Locate and identify every blood parasite.
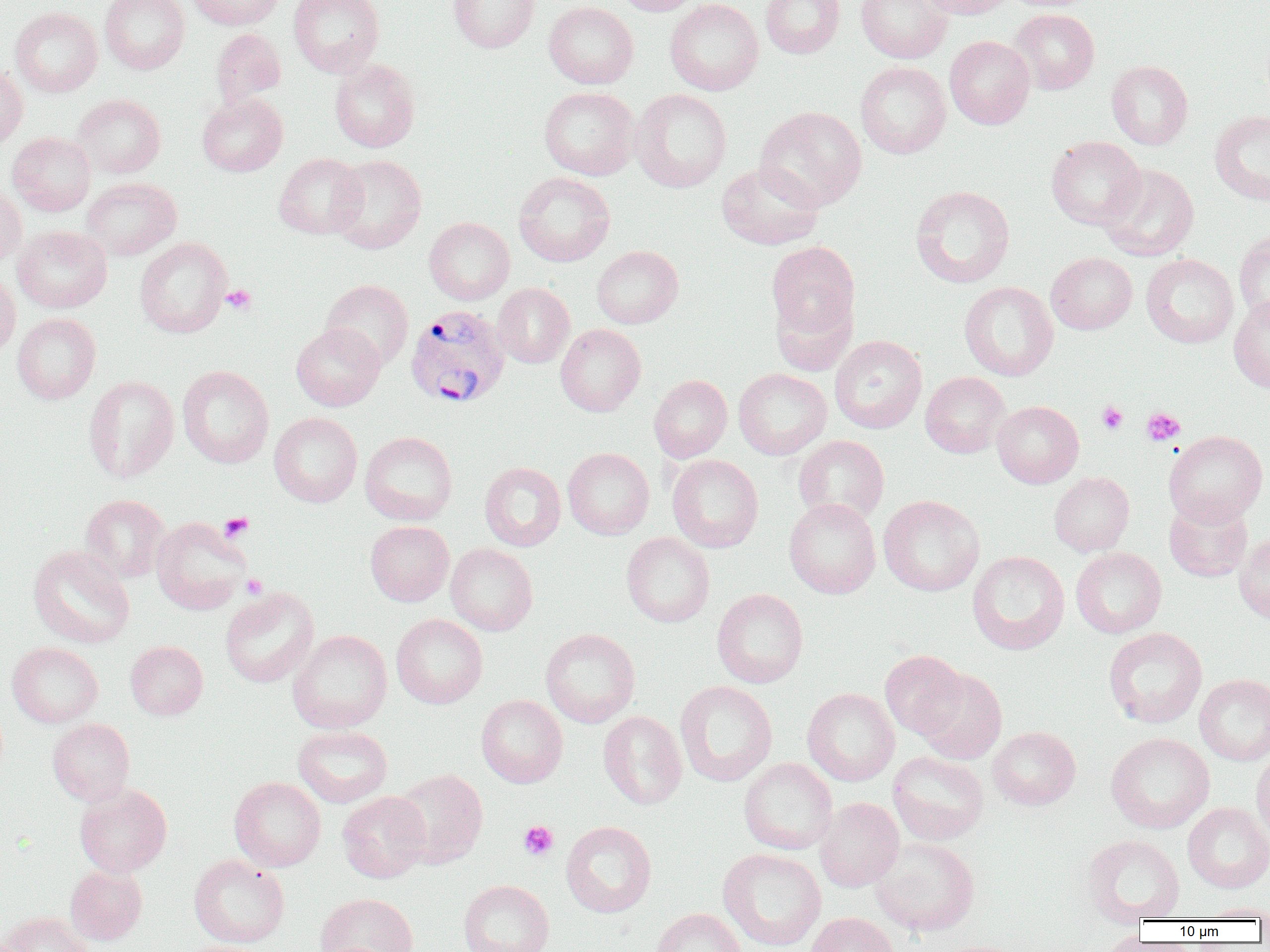
Approximate bounding boxes as (x1, y1, x2, y2) in pixels.
Plasmodium vivax-infected red blood cells: (405, 304, 511, 409).
No Plasmodium falciparum, Plasmodium ovale, Plasmodium malariae, Babesia divergens, or Trypanosoma brucei observed.

Uninfected red blood cell locations: (100, 0, 189, 74), (187, 0, 283, 29), (289, 0, 384, 77), (448, 0, 539, 53), (612, 0, 703, 16), (665, 0, 763, 95), (760, 0, 845, 58), (855, 0, 953, 63), (916, 0, 1015, 19), (543, 1, 639, 89), (10, 7, 103, 97), (1010, 9, 1100, 94), (211, 28, 286, 108), (944, 35, 1035, 129), (329, 59, 420, 152), (1106, 60, 1193, 150), (855, 61, 951, 159), (0, 65, 28, 153), (539, 87, 640, 180), (631, 89, 731, 193), (197, 93, 288, 177), (72, 94, 166, 178), (755, 106, 867, 211), (1210, 110, 1270, 205), (7, 132, 95, 216), (1046, 136, 1145, 230), (273, 153, 367, 239), (330, 154, 427, 254), (716, 163, 823, 250), (1098, 164, 1199, 261), (513, 172, 615, 267), (81, 177, 182, 260), (0, 184, 26, 269), (910, 186, 1014, 288), (424, 217, 515, 305), (13, 226, 112, 313), (1234, 230, 1270, 325), (134, 237, 232, 338), (765, 240, 860, 350), (591, 245, 683, 328), (1046, 252, 1137, 334), (1141, 254, 1238, 348), (0, 270, 21, 361), (320, 279, 414, 371), (959, 281, 1058, 381), (492, 283, 575, 368), (1229, 295, 1270, 392), (12, 313, 101, 404), (291, 323, 385, 411), (555, 324, 646, 416), (830, 335, 927, 433), (177, 365, 274, 468), (733, 368, 831, 460), (920, 372, 1010, 458), (83, 375, 179, 483), (648, 375, 732, 462), (992, 400, 1083, 488), (269, 412, 362, 507), (1164, 430, 1268, 525), (360, 431, 457, 525), (793, 435, 889, 525), (563, 447, 654, 539), (667, 454, 763, 553), (479, 462, 566, 551), (1049, 472, 1135, 556), (81, 494, 170, 582), (879, 495, 984, 596), (1164, 497, 1253, 582), (784, 498, 881, 599), (151, 517, 250, 614), (365, 521, 454, 606), (1234, 531, 1270, 624), (621, 532, 715, 627), (445, 544, 538, 636), (28, 545, 135, 649), (1071, 548, 1166, 638), (967, 551, 1070, 655), (220, 586, 319, 688), (712, 588, 808, 688), (391, 613, 488, 709), (1103, 627, 1207, 728), (540, 628, 640, 728), (288, 629, 392, 733), (125, 641, 208, 720), (7, 642, 103, 728), (879, 650, 967, 739), (915, 668, 1007, 764), (1195, 674, 1270, 765), (674, 680, 777, 787), (802, 688, 900, 786), (476, 694, 568, 788), (598, 711, 687, 809), (47, 718, 135, 806), (293, 725, 393, 807), (988, 726, 1080, 810), (1106, 732, 1214, 833), (1250, 749, 1270, 843), (888, 751, 989, 845), (739, 758, 838, 855), (391, 768, 489, 869), (229, 776, 326, 872), (74, 783, 172, 877), (337, 791, 431, 883), (815, 797, 904, 892), (1183, 802, 1270, 893), (561, 821, 657, 918), (1083, 834, 1185, 923), (870, 837, 980, 936), (718, 848, 826, 950), (189, 854, 289, 948), (65, 865, 147, 944), (458, 879, 554, 952), (315, 892, 418, 952), (1199, 902, 1270, 920), (651, 907, 746, 952), (2, 911, 94, 952), (806, 912, 900, 952). Platelet locations: (222, 284, 256, 314), (1097, 400, 1128, 434), (1141, 407, 1185, 446), (218, 513, 254, 542), (241, 574, 267, 599), (518, 821, 559, 860). Slide-level diagnosis: Plasmodium vivax. Thin blood film. Image is 1270×952 pixels. Optical microscopy. Captured at 1000x magnification. One field of a larger specimen.